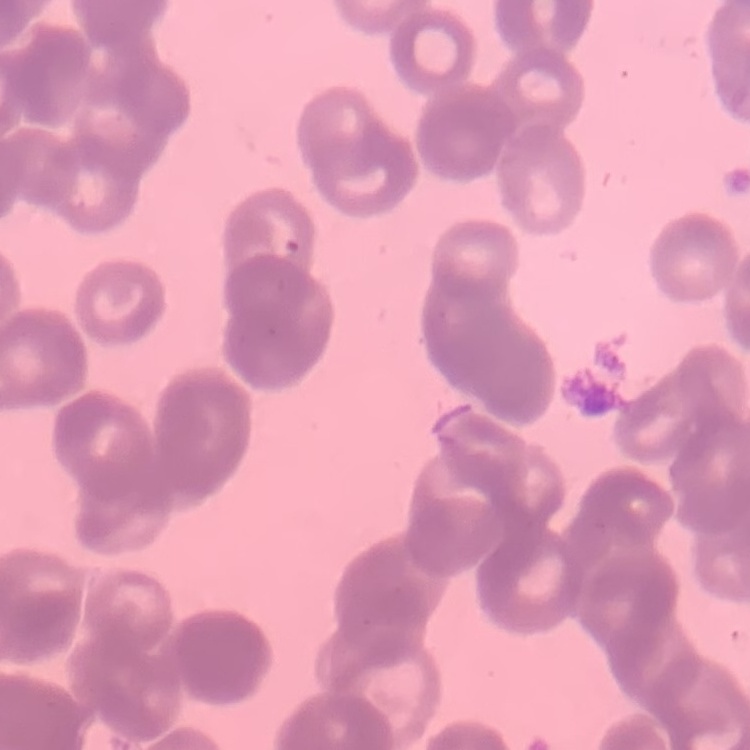

Summary:
  - Erythrocyte morphology: rouleaux formation
  - Image type: square crop of a larger photomicrograph
  - Preparation: thin peripheral smear
  - Stain: Field's or Giemsa